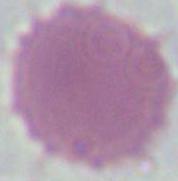 A red blood cell is seen. Micrograph. Captured at 1000x magnification.